Assess this cell for malaria.
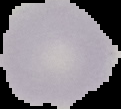
It is uninfected.

Image is 121×109 pixels. Segmented cell region on a black background. From a thin blood smear.